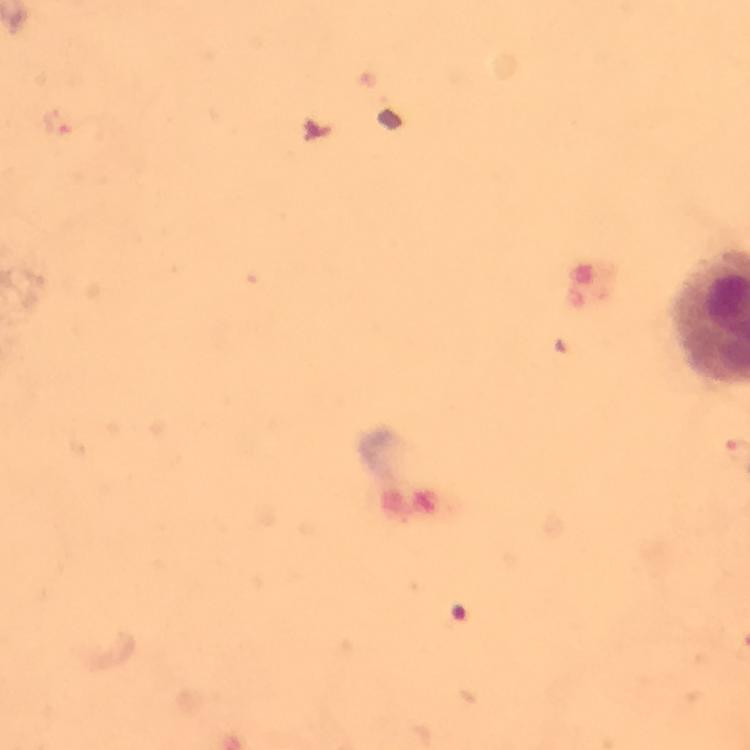

Approximate centers as (x, y) in pixels.
Summary:
  - Plasmodium parasite locations: (61, 121)
  - Magnification: 100x
  - Immersion oil: used
  - Preparation: thick blood smear
  - Capture: smartphone camera through the microscope
  - Cropped from: a single field of view
  - Stain: Giemsa
  - Context: from a diagnostic examination for malaria
  - Image size: 750×750 pixels